Report the malaria status.
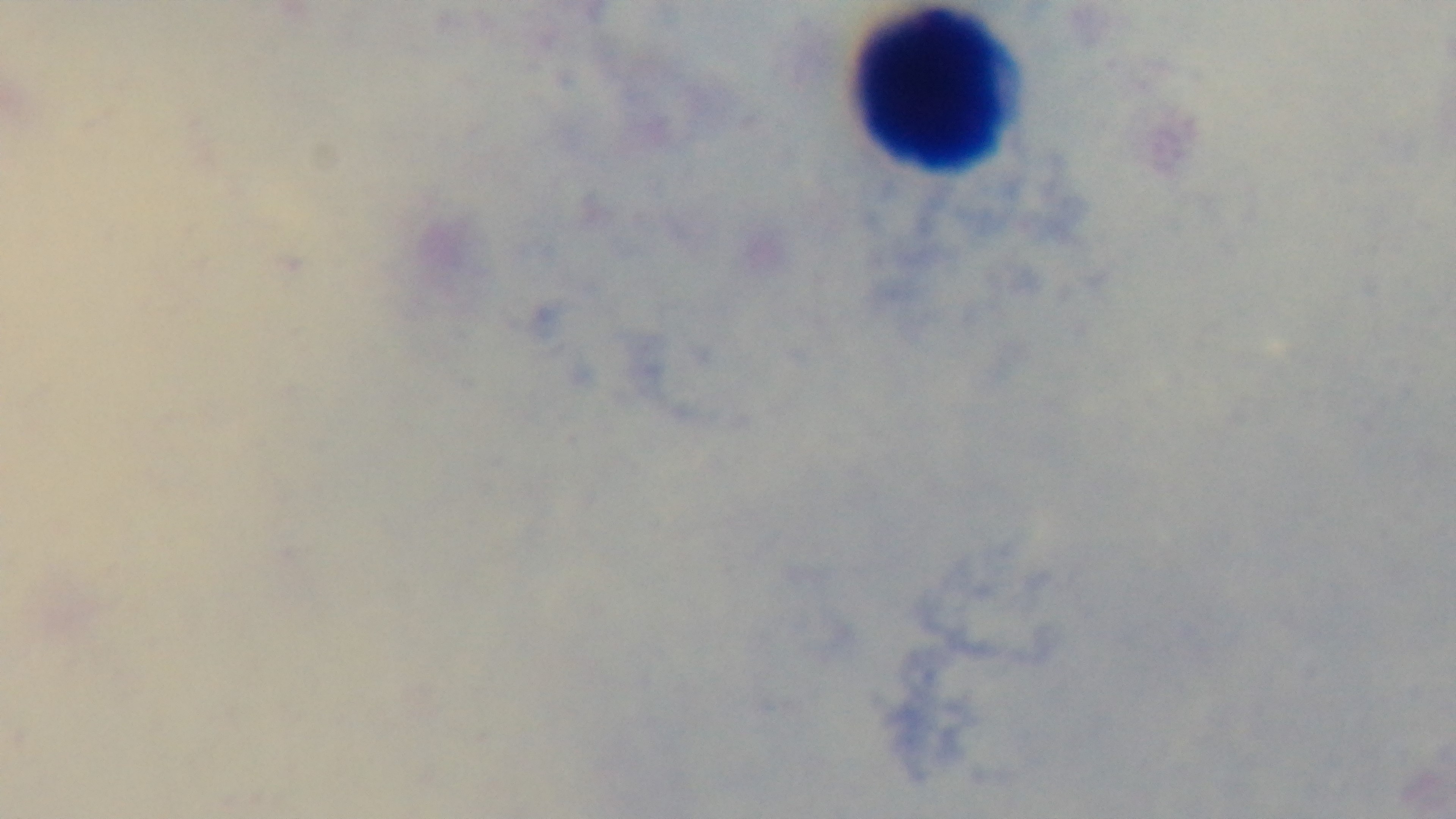
Uninfected.

Mounted 4K digital camera. 100x oil-immersion objective. Preparation: thick. Photomicrograph. Giemsa-stained. One field from the slide.